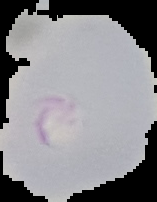

image size = 157×202 pixels
result = Plasmodium parasites identified
preparation = thin blood film
image type = segmented cell region with the area outside set to black